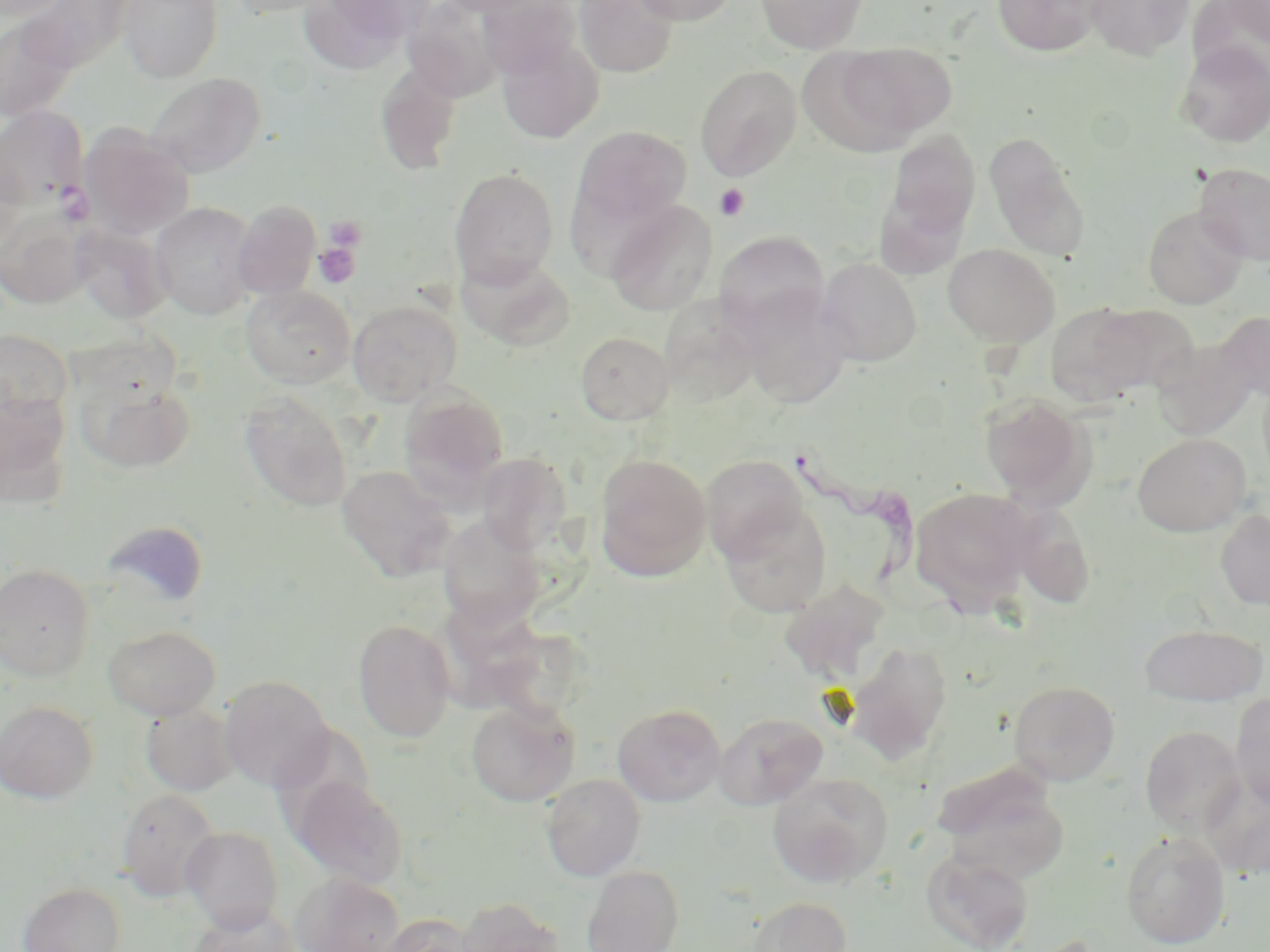
Summary:
  - Coordinate format: approximate bounding boxes as (x1,y1)-(x2,y2) corner pairs in pixels
  - Trypanosoma brucei locations: (795,441)-(950,622)
  - Uninfected red blood cell locations: (115,0)-(225,83), (224,0)-(341,18), (320,0)-(438,42), (437,0)-(553,17), (574,0)-(679,78), (631,0)-(738,26), (756,0)-(868,53), (993,0)-(1102,57), (1085,0)-(1194,60), (1216,0)-(1270,46), (300,1)-(423,72), (402,1)-(506,102), (476,1)-(581,79), (0,15)-(82,123), (495,34)-(605,144), (1176,42)-(1270,147), (831,43)-(956,143), (375,62)-(463,175), (694,65)-(801,181), (144,72)-(266,178), (0,106)-(88,208), (79,124)-(195,239), (570,125)-(692,234), (881,129)-(981,248), (983,132)-(1089,259), (0,147)-(27,255), (1194,162)-(1270,265), (449,167)-(559,289), (232,199)-(321,300), (606,199)-(718,316), (150,202)-(258,320), (0,206)-(96,309), (1143,206)-(1248,309), (72,224)-(172,323), (714,230)-(829,335), (943,244)-(1058,347), (457,251)-(576,351), (816,257)-(921,367), (241,285)-(356,388), (736,286)-(853,409), (660,298)-(762,407), (347,299)-(462,405), (1045,302)-(1150,405), (1089,304)-(1200,396), (1216,311)-(1270,401), (0,329)-(73,424), (575,332)-(674,425), (1150,339)-(1257,440), (74,374)-(197,474), (398,386)-(510,504), (0,387)-(72,508), (239,391)-(353,511), (980,392)-(1096,507), (1132,433)-(1252,537), (477,452)-(572,554), (594,453)-(712,580), (700,454)-(810,562), (337,465)-(457,582), (909,487)-(1037,615), (718,502)-(832,618), (1009,503)-(1096,610), (1214,508)-(1270,611), (437,516)-(547,631), (100,520)-(209,612), (0,563)-(96,681), (780,579)-(891,684), (353,619)-(456,742), (451,619)-(586,722), (103,624)-(221,720), (1138,624)-(1268,705), (844,641)-(953,764), (219,675)-(334,791), (1008,680)-(1120,785), (1230,693)-(1270,809), (0,700)-(99,803), (466,701)-(579,806), (140,703)-(239,796), (612,703)-(726,806), (714,711)-(828,810), (1140,725)-(1247,836), (935,766)-(1070,885), (541,773)-(646,881), (768,773)-(893,887), (290,775)-(408,888), (1206,778)-(1270,881), (115,789)-(221,902), (181,826)-(284,933), (1120,830)-(1231,949), (921,848)-(1033,951), (581,865)-(683,952), (290,873)-(406,951), (18,882)-(126,952), (746,896)-(852,952), (456,897)-(565,952), (190,905)-(301,952), (379,913)-(481,952)
  - Platelet locations: (714,184)-(750,221), (323,215)-(367,254), (313,241)-(362,289)
  - Slide-level diagnosis: Trypanosoma brucei
  - Field of view: one of a larger specimen
  - Modality: optical microscopy
  - Preparation: thin blood film
  - Image size: 1270×952 pixels
  - Stain: May-Grünwald-Giemsa
  - Magnification: 1000x